State which cell type is depicted.
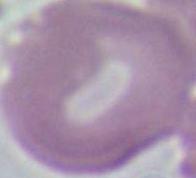
This is an erythrocyte.

Photomicrograph. Captured at 1000x magnification.